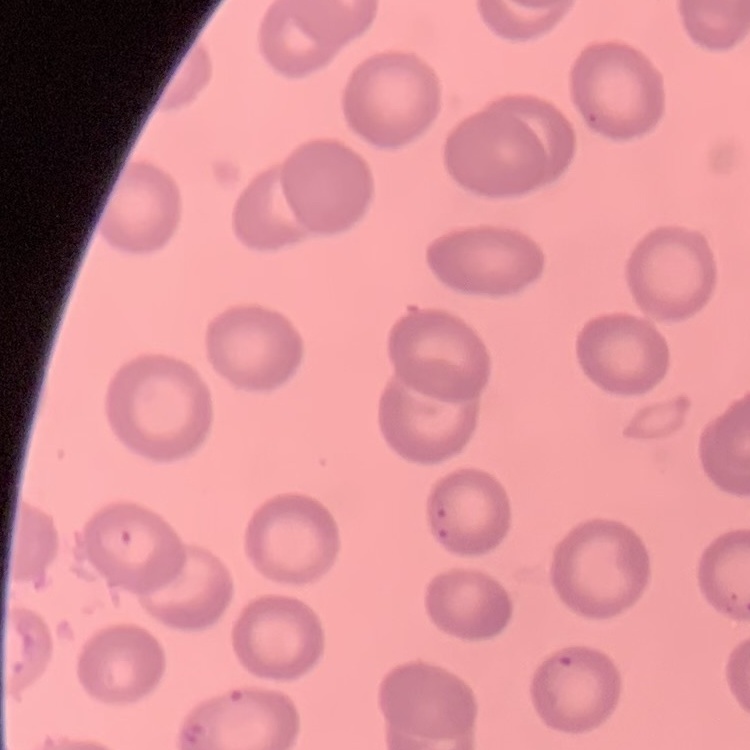
{
  "erythrocyte_morphology": "no rouleaux formation",
  "image_type": "one tile cut from a larger photomicrograph",
  "preparation": "thin blood film",
  "stain": "Field's or Giemsa"
}